Give the extent of all Plasmodium vivax-infected red blood cells.
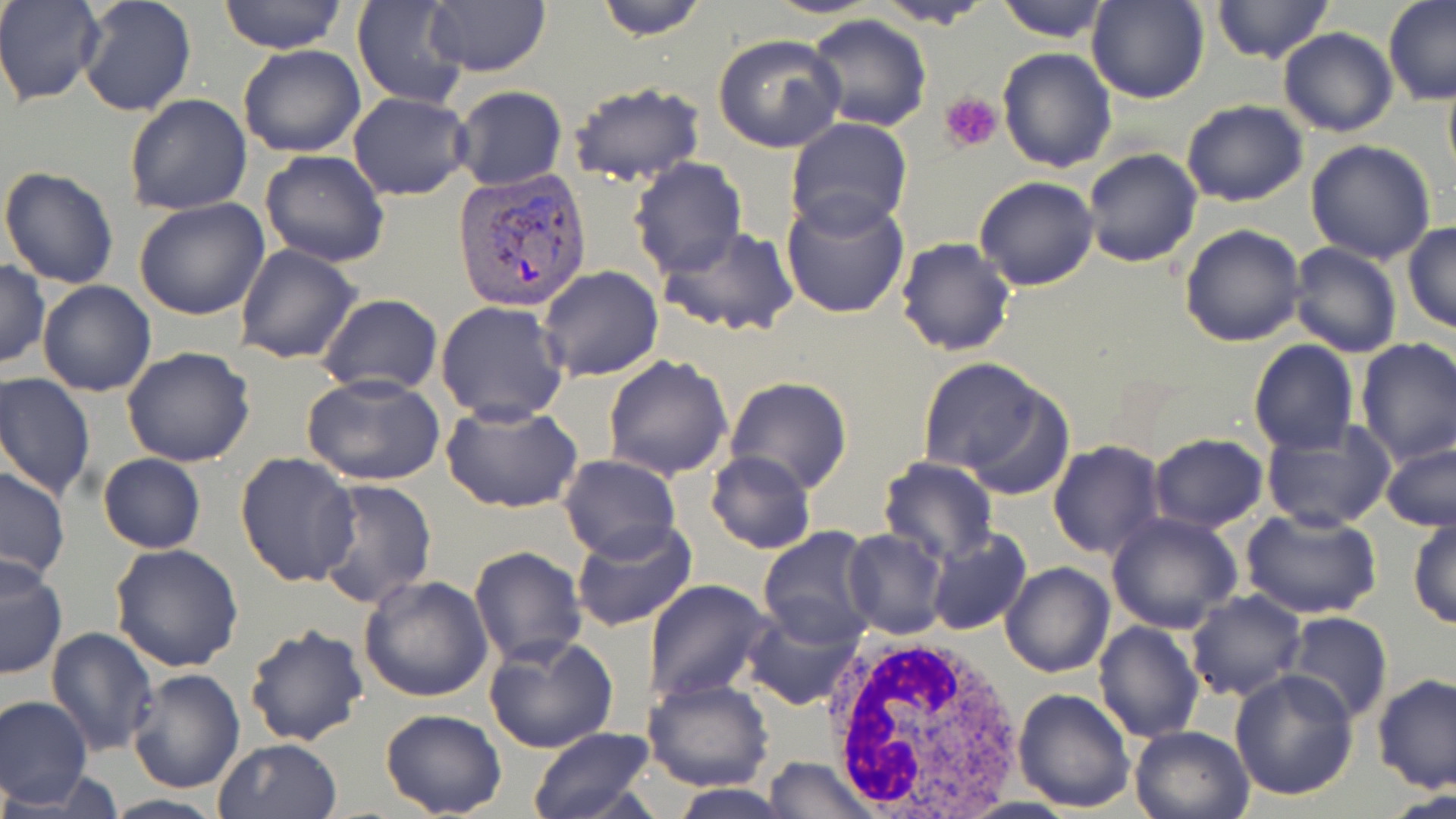
Approximate bounding boxes as named x1/y1/x2/y2 corners in pixels.
Plasmodium vivax-infected red blood cells: (x1=454, y1=168, x2=592, y2=310).

slide_level_diagnosis: Plasmodium vivax
modality: optical microscopy
platelet_locations: 'approximate bounding boxes as named x1/y1/x2/y2 corners in pixels: (x1=940, y1=90, x2=1002, y2=153)'
white_blood_cell_locations: 'approximate bounding boxes as named x1/y1/x2/y2 corners in pixels: (x1=820, y1=630, x2=1027, y2=811)'
preparation: thin blood smear
magnification: 1000x
field_of_view: one of a larger specimen
image_size: 1456×819 pixels
stain: May-Grünwald-Giemsa
uninfected_red_blood_cell_locations: 'approximate bounding boxes as named x1/y1/x2/y2 corners in pixels: (x1=0, y1=0, x2=103, y2=104), (x1=77, y1=0, x2=197, y2=118), (x1=217, y1=0, x2=347, y2=54), (x1=352, y1=0, x2=469, y2=109), (x1=593, y1=0, x2=712, y2=39), (x1=874, y1=0, x2=995, y2=29), (x1=995, y1=0, x2=1112, y2=43), (x1=1087, y1=0, x2=1212, y2=104), (x1=1210, y1=0, x2=1335, y2=64), (x1=1383, y1=1, x2=1456, y2=105), (x1=424, y1=3, x2=551, y2=77), (x1=802, y1=13, x2=932, y2=132), (x1=1278, y1=28, x2=1397, y2=137), (x1=713, y1=34, x2=845, y2=153), (x1=238, y1=45, x2=365, y2=158), (x1=996, y1=46, x2=1118, y2=173), (x1=1442, y1=73, x2=1456, y2=183), (x1=567, y1=82, x2=707, y2=188), (x1=453, y1=86, x2=566, y2=191), (x1=347, y1=92, x2=474, y2=200), (x1=124, y1=94, x2=252, y2=216), (x1=1181, y1=100, x2=1309, y2=206), (x1=785, y1=117, x2=912, y2=236), (x1=1305, y1=140, x2=1438, y2=264), (x1=1082, y1=146, x2=1203, y2=269), (x1=260, y1=150, x2=390, y2=268), (x1=629, y1=157, x2=746, y2=277), (x1=1, y1=166, x2=119, y2=289), (x1=975, y1=175, x2=1101, y2=291), (x1=781, y1=189, x2=910, y2=319), (x1=133, y1=197, x2=271, y2=320), (x1=1403, y1=222, x2=1456, y2=333), (x1=1178, y1=224, x2=1306, y2=348), (x1=657, y1=226, x2=799, y2=337), (x1=894, y1=237, x2=1016, y2=356), (x1=1288, y1=242, x2=1403, y2=357), (x1=235, y1=243, x2=363, y2=366), (x1=0, y1=261, x2=49, y2=369), (x1=538, y1=266, x2=663, y2=382), (x1=37, y1=280, x2=157, y2=398), (x1=316, y1=293, x2=441, y2=397), (x1=435, y1=300, x2=570, y2=423), (x1=1355, y1=336, x2=1456, y2=464), (x1=1248, y1=340, x2=1359, y2=454), (x1=122, y1=345, x2=256, y2=466), (x1=602, y1=354, x2=732, y2=480), (x1=915, y1=357, x2=1058, y2=482), (x1=1, y1=372, x2=97, y2=500), (x1=300, y1=373, x2=449, y2=490), (x1=724, y1=377, x2=853, y2=494), (x1=441, y1=401, x2=586, y2=514), (x1=1260, y1=417, x2=1395, y2=532), (x1=1149, y1=432, x2=1269, y2=532), (x1=1048, y1=440, x2=1166, y2=560), (x1=1382, y1=442, x2=1456, y2=531), (x1=707, y1=451, x2=815, y2=554), (x1=234, y1=452, x2=361, y2=588), (x1=98, y1=454, x2=204, y2=553), (x1=558, y1=454, x2=681, y2=561), (x1=878, y1=456, x2=999, y2=565), (x1=0, y1=466, x2=71, y2=586), (x1=311, y1=479, x2=438, y2=612), (x1=1241, y1=508, x2=1384, y2=620), (x1=1106, y1=511, x2=1243, y2=634), (x1=1407, y1=515, x2=1455, y2=629), (x1=570, y1=518, x2=697, y2=633), (x1=757, y1=527, x2=877, y2=646), (x1=925, y1=528, x2=1032, y2=637), (x1=842, y1=529, x2=949, y2=640), (x1=110, y1=541, x2=244, y2=671), (x1=468, y1=546, x2=588, y2=667), (x1=0, y1=555, x2=66, y2=680), (x1=1002, y1=563, x2=1115, y2=678), (x1=358, y1=575, x2=494, y2=703), (x1=644, y1=578, x2=773, y2=702), (x1=1187, y1=592, x2=1306, y2=703), (x1=741, y1=602, x2=866, y2=713), (x1=1282, y1=611, x2=1393, y2=724), (x1=1093, y1=620, x2=1205, y2=744), (x1=244, y1=622, x2=370, y2=748), (x1=45, y1=626, x2=158, y2=755), (x1=484, y1=634, x2=619, y2=754), (x1=125, y1=668, x2=246, y2=795), (x1=1229, y1=669, x2=1358, y2=801), (x1=1373, y1=674, x2=1455, y2=791), (x1=642, y1=678, x2=773, y2=791), (x1=1013, y1=686, x2=1138, y2=812), (x1=0, y1=695, x2=92, y2=807), (x1=379, y1=708, x2=507, y2=818), (x1=1129, y1=724, x2=1254, y2=818), (x1=524, y1=727, x2=656, y2=819), (x1=213, y1=738, x2=343, y2=819), (x1=763, y1=756, x2=879, y2=819), (x1=669, y1=785, x2=796, y2=817), (x1=100, y1=795, x2=229, y2=819)'